Name the blood parasite species.
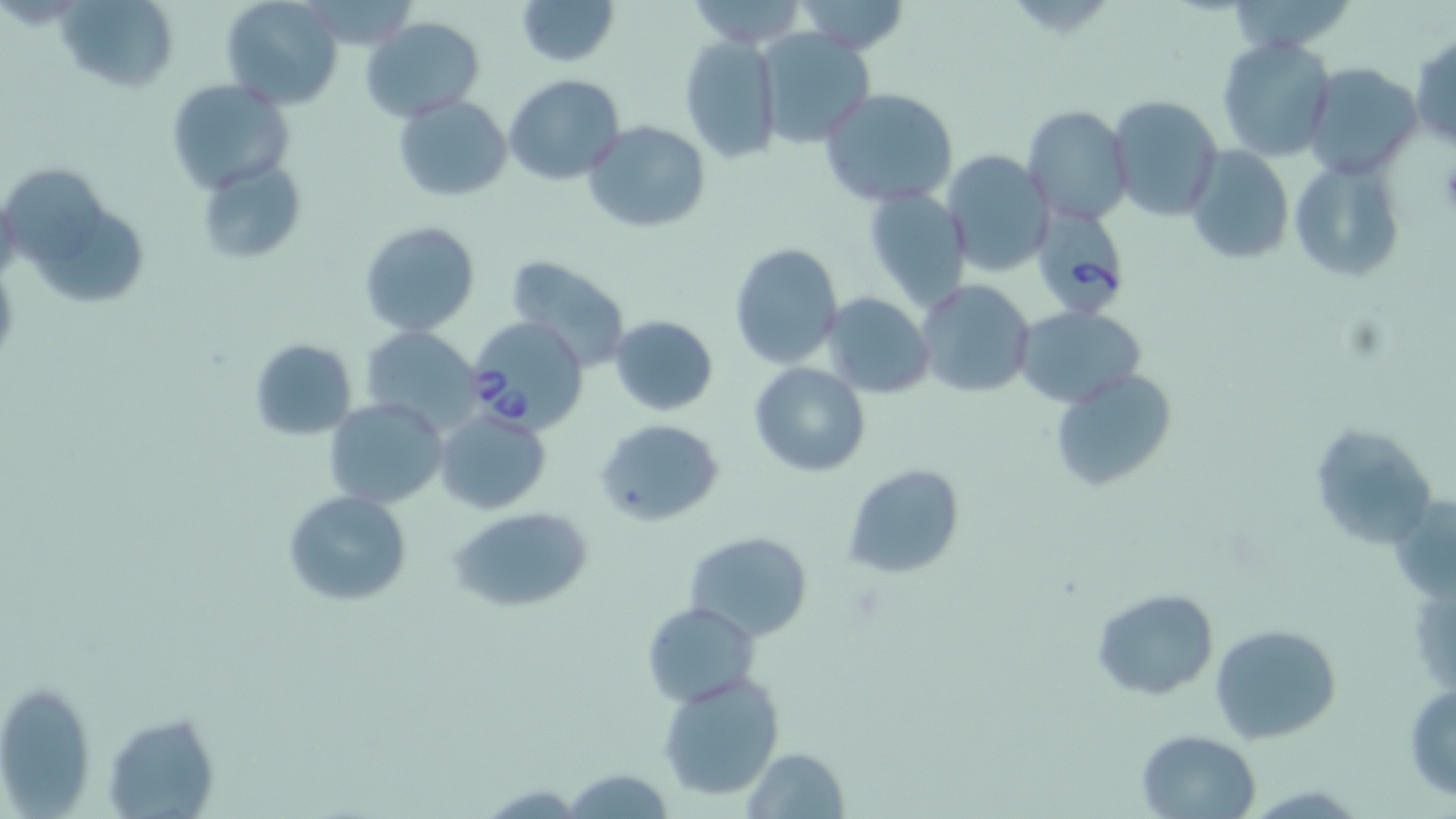

Babesia divergens.

Approximate bounding boxes as (x1, y1, x2, y2) in pixels. Uninfected red blood cell locations: (58, 0, 177, 92), (220, 0, 342, 109), (516, 0, 619, 67), (681, 0, 810, 47), (790, 0, 914, 54), (1233, 0, 1348, 57), (361, 16, 484, 121), (756, 30, 876, 149), (679, 35, 782, 163), (1410, 35, 1456, 150), (1217, 36, 1338, 160), (1304, 63, 1423, 181), (505, 75, 626, 185), (166, 79, 293, 194), (820, 88, 959, 208), (393, 95, 511, 201), (1106, 95, 1223, 223), (1022, 105, 1135, 227), (583, 121, 711, 234), (1185, 145, 1294, 267), (939, 150, 1054, 278), (1288, 154, 1408, 283), (194, 159, 304, 266), (2, 165, 107, 267), (863, 185, 973, 310), (36, 210, 152, 305), (360, 219, 480, 337), (730, 243, 843, 369), (505, 255, 630, 371), (916, 278, 1035, 399), (821, 292, 935, 398), (1015, 306, 1147, 408), (609, 315, 719, 415), (363, 328, 482, 436), (248, 339, 358, 439), (749, 362, 869, 476), (1049, 368, 1178, 494), (324, 398, 448, 509), (434, 406, 552, 515), (595, 417, 725, 526), (1310, 424, 1438, 554), (844, 465, 964, 579), (284, 491, 411, 605), (447, 504, 597, 613), (684, 531, 812, 642), (1091, 588, 1219, 699), (644, 601, 757, 704), (1210, 624, 1342, 744), (657, 673, 785, 802), (1, 680, 97, 813), (1404, 686, 1456, 801), (101, 710, 221, 818), (1134, 729, 1260, 817), (739, 747, 849, 818), (563, 766, 673, 818). Babesia divergens-infected red blood cell locations: (1040, 207, 1135, 318), (466, 318, 587, 436). One field of a larger specimen. Image is 1456×819 pixels. Optical microscopy. Thin blood smear. May-Grünwald-Giemsa-stained preparation. 1000x magnification.